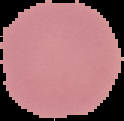
{
  "preparation": "thin blood smear",
  "malaria_status": "uninfected",
  "image_type": "cell region segmented out of the field of view; surrounding area masked to black",
  "image_size": "124×121 pixels"
}